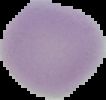

Malaria status: uninfected. From a thin blood film. Segmented cell region on a black background. Image is 106×100 pixels.